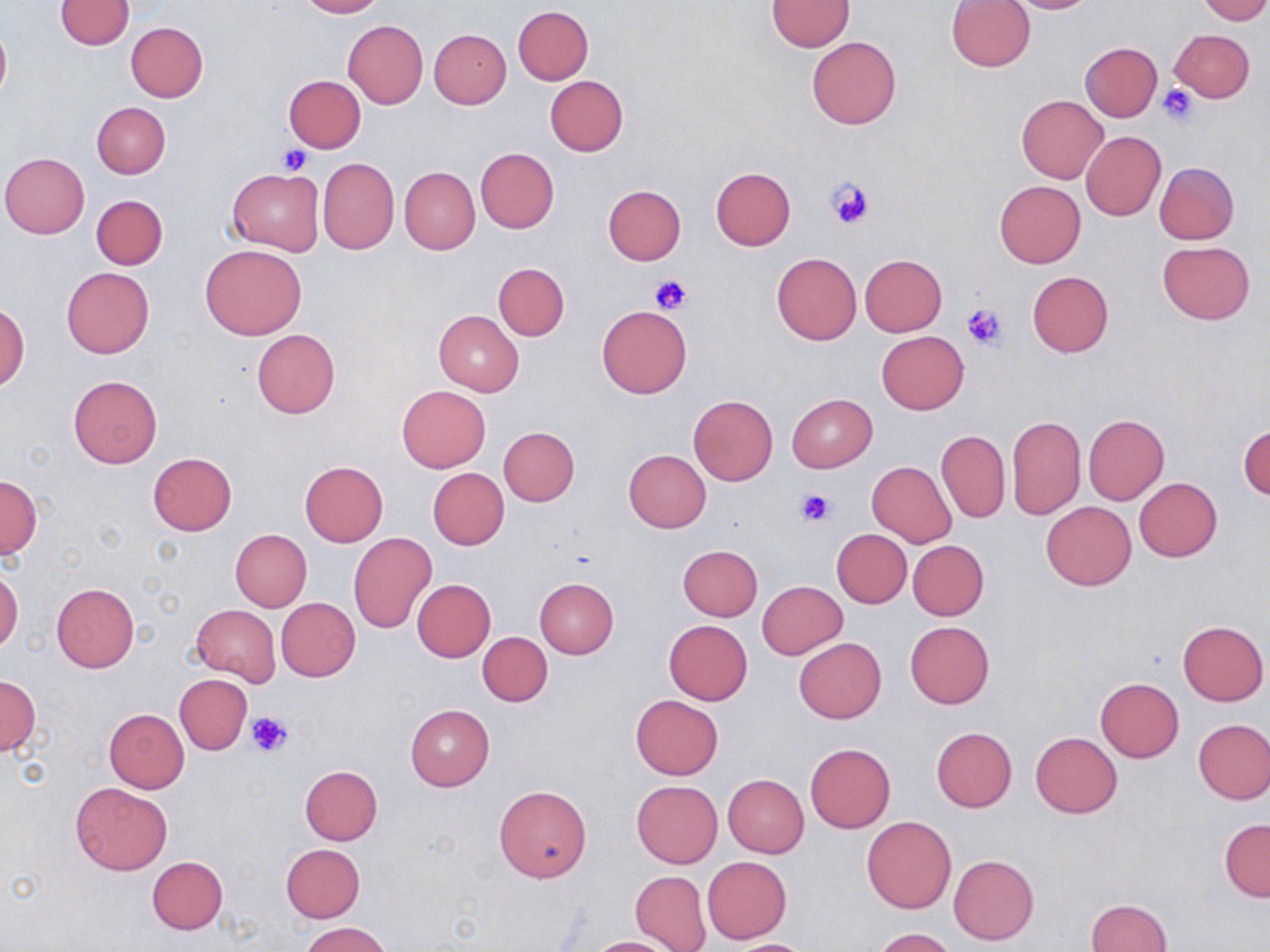

Summary:
  - Coordinate format: approximate bounding boxes as [x1, y1, x2, y2] in pixels
  - Uninfected red blood cell locations: [55, 0, 134, 50], [296, 0, 385, 17], [947, 0, 1035, 72], [1002, 0, 1099, 14], [1198, 0, 1270, 24], [766, 1, 853, 51], [513, 5, 593, 84], [344, 20, 428, 108], [0, 21, 11, 105], [125, 21, 208, 101], [430, 28, 511, 108], [1169, 29, 1254, 103], [806, 37, 900, 129], [1079, 42, 1162, 121], [284, 75, 365, 153], [544, 76, 628, 156], [1016, 94, 1108, 183], [92, 101, 170, 178], [1081, 131, 1166, 220], [476, 148, 558, 232], [1, 152, 89, 238], [317, 157, 399, 255], [1154, 162, 1238, 243], [400, 166, 479, 254], [709, 166, 796, 250], [227, 168, 324, 254], [994, 180, 1086, 268], [604, 185, 686, 264], [91, 194, 167, 269], [1157, 242, 1254, 324], [201, 243, 308, 340], [771, 253, 861, 345], [860, 255, 946, 336], [494, 263, 569, 341], [62, 268, 154, 358], [1026, 271, 1114, 357], [0, 302, 29, 392], [598, 305, 691, 397], [434, 310, 523, 397], [252, 329, 340, 418], [876, 331, 968, 414], [68, 375, 162, 469], [398, 386, 490, 471], [787, 393, 877, 472], [688, 396, 778, 485], [1007, 415, 1085, 520], [1083, 415, 1169, 504], [1239, 423, 1269, 502], [498, 427, 579, 506], [937, 430, 1010, 523], [624, 449, 711, 531], [148, 452, 236, 535], [299, 461, 389, 546], [868, 463, 957, 547], [428, 468, 509, 551], [0, 475, 40, 557], [1134, 477, 1222, 561], [1041, 502, 1136, 589], [831, 529, 911, 607], [231, 530, 312, 611], [349, 532, 435, 632], [908, 540, 988, 621], [678, 545, 762, 620], [0, 566, 21, 656], [534, 576, 618, 658], [413, 579, 496, 662], [757, 581, 847, 658], [51, 584, 140, 673], [276, 597, 361, 682], [190, 605, 281, 688], [663, 620, 752, 705], [1177, 620, 1268, 706], [905, 621, 994, 708], [478, 632, 552, 706], [794, 637, 887, 723], [174, 674, 252, 755], [0, 676, 41, 758], [1095, 677, 1183, 762], [631, 695, 724, 779], [404, 704, 494, 790], [104, 708, 188, 793], [1193, 719, 1270, 804], [931, 727, 1017, 811], [1031, 731, 1122, 817], [805, 744, 895, 833], [299, 765, 383, 845], [723, 774, 808, 858], [70, 781, 172, 875], [632, 781, 722, 867], [494, 784, 593, 883], [861, 816, 956, 913], [1219, 818, 1269, 901], [280, 843, 365, 923], [948, 854, 1039, 945], [148, 856, 228, 934], [702, 857, 792, 943], [631, 871, 710, 951], [1084, 899, 1172, 952], [300, 921, 392, 952], [872, 927, 958, 952], [582, 936, 682, 951], [721, 939, 817, 951]
  - Platelet locations: [1157, 84, 1200, 126], [279, 145, 312, 176], [828, 176, 876, 230], [649, 274, 692, 314], [961, 302, 1009, 351], [796, 488, 835, 526], [247, 712, 293, 760]
  - Slide-level diagnosis: no evidence of blood parasites
  - Image size: 1270×952 pixels
  - Preparation: thin blood film
  - Stain: May-Grünwald-Giemsa
  - Field of view: one of a larger specimen
  - Modality: light microscopy
  - Magnification: 1000x